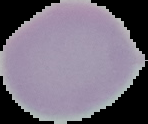 Image is 148×124 pixels. Result: no malaria parasites detected. From a thin blood smear. Cell region segmented out of the field of view; the surrounding area is masked to black.